State which parasite is depicted.
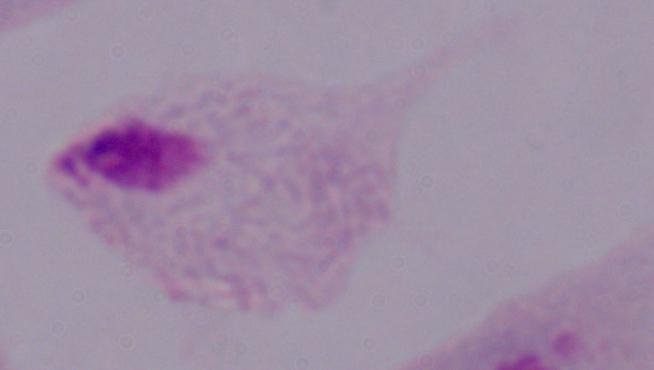

A trichomonad.

Summary:
  - Magnification: 1000x
  - Modality: photomicrograph